Evaluate for malaria.
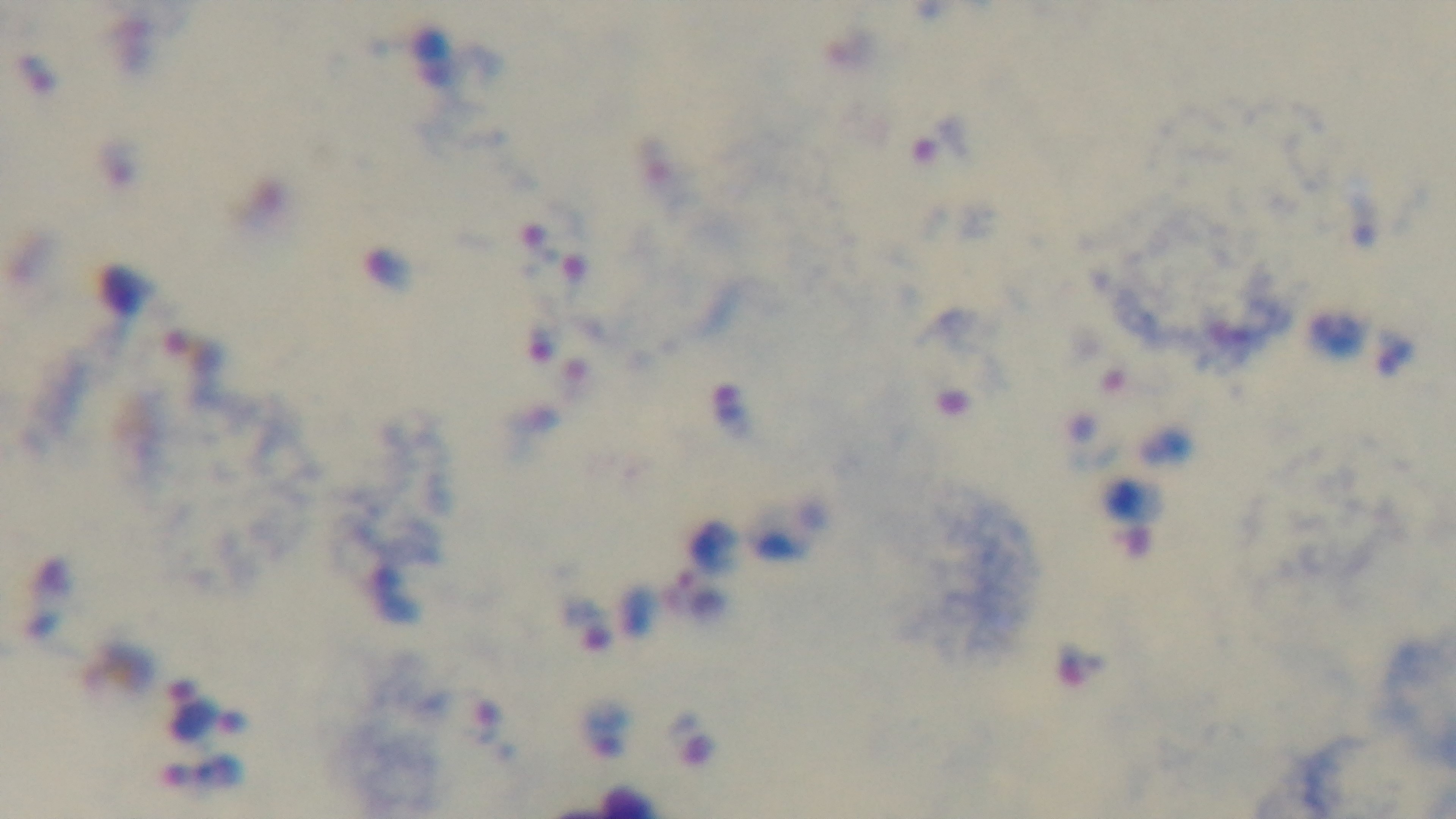

Positive.

stain = Giemsa
capture = mounted 4K digital camera
preparation = thick
modality = light microscopy
field of view = one from the slide
objective = 100x oil immersion